Report the malaria status of this cell.
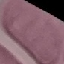

It is uninfected.

{
  "preparation": "thin smear",
  "capture": "smartphone through the microscope eyepiece",
  "image_type": "automatically extracted cell patch, resized to 64 × 64 pixels",
  "stain": "Giemsa"
}